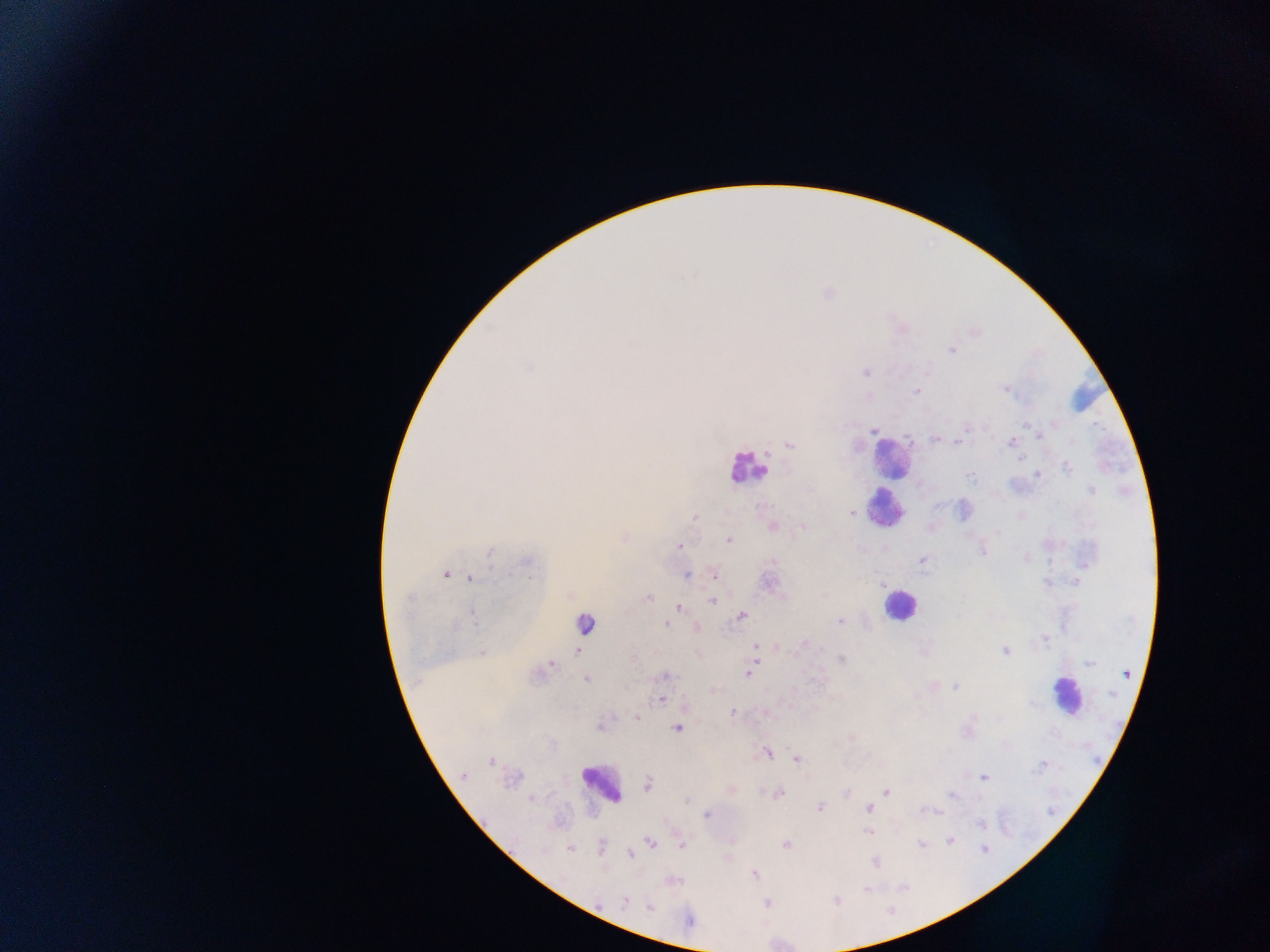

Approximate centers as x y in pixels.
Summary:
  - Leukocyte locations: 1080 392; 891 456; 747 468; 884 508; 894 605; 586 623; 1065 695; 601 782
  - Plasmodium parasite locations: 692 274; 952 350; 530 367; 866 372; 1005 389; 917 391; 1027 425; 967 427; 874 430; 1038 435; 935 439; 1011 442; 958 443; 790 445; 1019 459; 1068 467; 1037 475; 971 477; 1091 491; 852 514; 1021 515; 695 516; 773 526; 803 527; 998 533; 729 540; 680 546; 982 550; 490 552; 1026 557; 923 559; 528 561; 773 561; 446 574; 686 575; 715 576; 471 578; 1076 581; 649 597; 407 599; 712 601; 679 607; 741 615; 474 617; 959 617; 840 621; 667 624; 455 625; 696 628; 1044 639; 804 643; 755 647; 1004 650; 577 651; 482 653; 633 658; 841 659; 756 661; 1089 663; 550 664; 747 674; 1127 674; 664 676; 586 680; 956 687; 915 696; 661 700; 732 713; 636 718; 599 727; 678 728; 851 738; 767 752; 797 759; 491 762; 1043 765; 463 776; 984 777; 514 780; 648 784; 886 792; 847 793; 779 794; 952 796; 532 799; 686 801; 820 808; 869 808; 936 812; 706 815; 981 824; 868 832; 950 841; 651 843; 921 844; 681 845; 785 845; 601 846; 570 849; 984 849; 630 854; 876 863; 754 874; 674 880; 866 889; 625 901; 837 902; 766 904; 650 907; 689 921
  - Country: Ghana
  - Capture: mobile-phone photograph through a microscope
  - Preparation: thick blood smear
  - Image size: 1270×952 pixels
  - Field of view: single